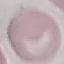
malaria status = uninfected
image type = cell patch, automatically extracted from a larger field of view and resized to 64 × 64 pixels
capture = smartphone through the microscope eyepiece
preparation = thin blood film
stain = Giemsa